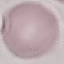
malaria status = uninfected
preparation = thin blood smear
stain = Giemsa
image type = automatically extracted cell patch, resized to 64 × 64 pixels
capture = smartphone through the microscope eyepiece